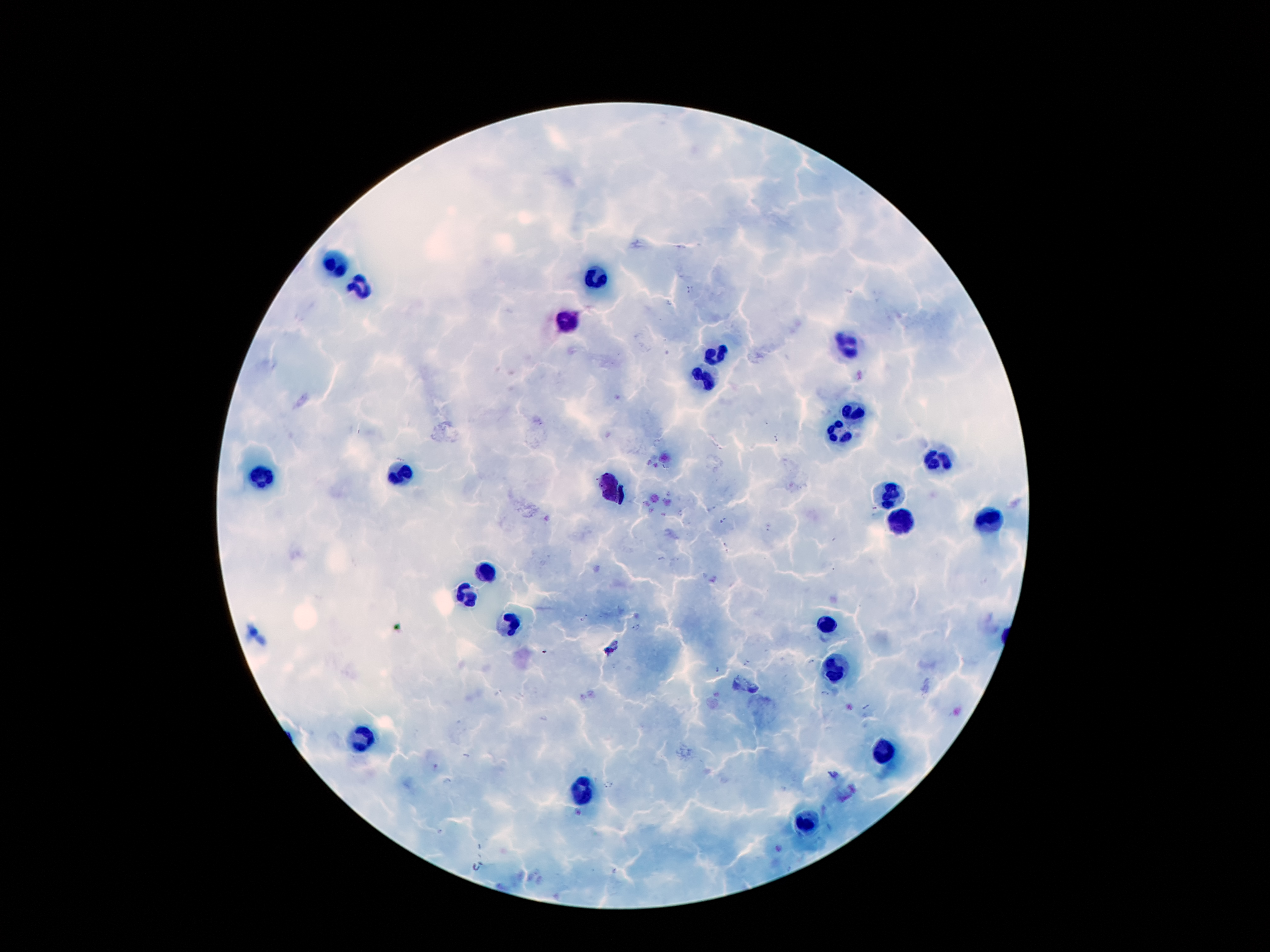

{
  "capture": "smartphone camera through the microscope eyepiece",
  "image_size": "1270×952 pixels",
  "malaria_parasite_locations": "approximate centers as {x, y} in pixels: {689, 289}, {669, 303}, {775, 438}, {664, 467}, {668, 494}, {874, 508}, {712, 509}, {679, 513}, {723, 521}, {768, 527}, {724, 542}, {728, 553}, {661, 559}, {584, 619}, {636, 628}, {811, 662}, {746, 663}, {717, 668}, {825, 694}, {579, 813}, {615, 870}",
  "field_of_view": "single",
  "leukocyte_locations": "approximate centers as {x, y} in pixels: {337, 264}, {592, 279}, {363, 289}, {566, 322}, {846, 346}, {714, 356}, {702, 376}, {852, 412}, {839, 434}, {940, 458}, {398, 475}, {262, 481}, {613, 494}, {889, 494}, {988, 520}, {900, 525}, {486, 572}, {467, 598}, {510, 624}, {829, 624}, {837, 667}, {361, 736}, {880, 753}, {581, 794}, {809, 822}",
  "preparation": "thick peripheral-blood smear",
  "magnification": "100x",
  "patient_malaria_status": "infected with Plasmodium falciparum",
  "stain": "Giemsa"
}